Point out each leukocyte.
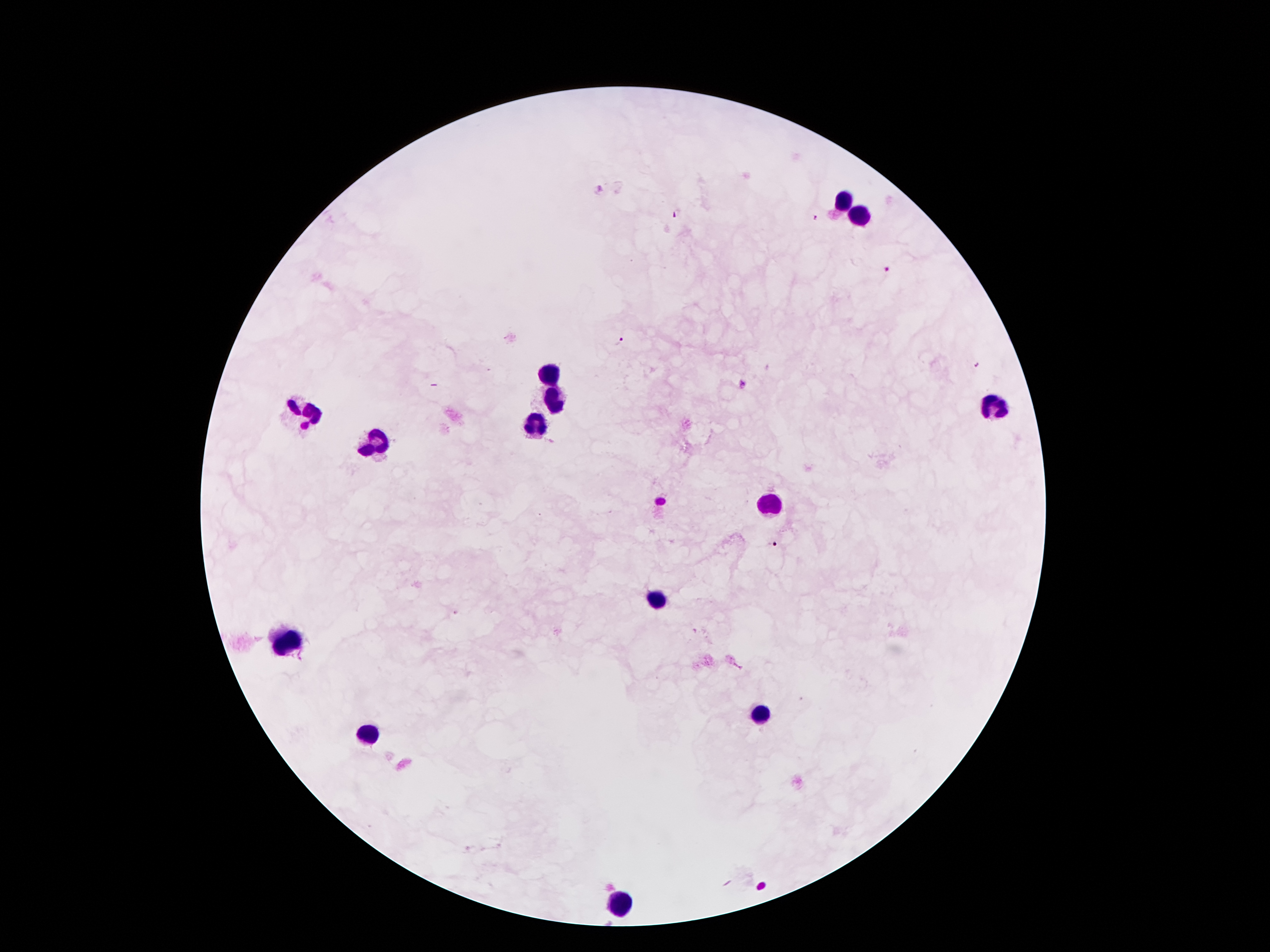

Approximate centers as [x, y] in pixels.
Leukocytes: [845, 198], [857, 215], [548, 372], [554, 398], [993, 409], [304, 413], [533, 424], [375, 445], [771, 505], [657, 600], [291, 639], [761, 715], [373, 732], [618, 902].

Summary:
  - Malaria parasite locations: [598, 190], [678, 213], [816, 219], [888, 270], [621, 340], [976, 366], [741, 388], [772, 546]
  - Patient malaria status: infected with Plasmodium falciparum
  - Preparation: thick blood smear
  - Field of view: one from this slide
  - Capture: smartphone through the microscope eyepiece
  - Image size: 1270×952 pixels
  - Stain: Giemsa
  - Magnification: 100x